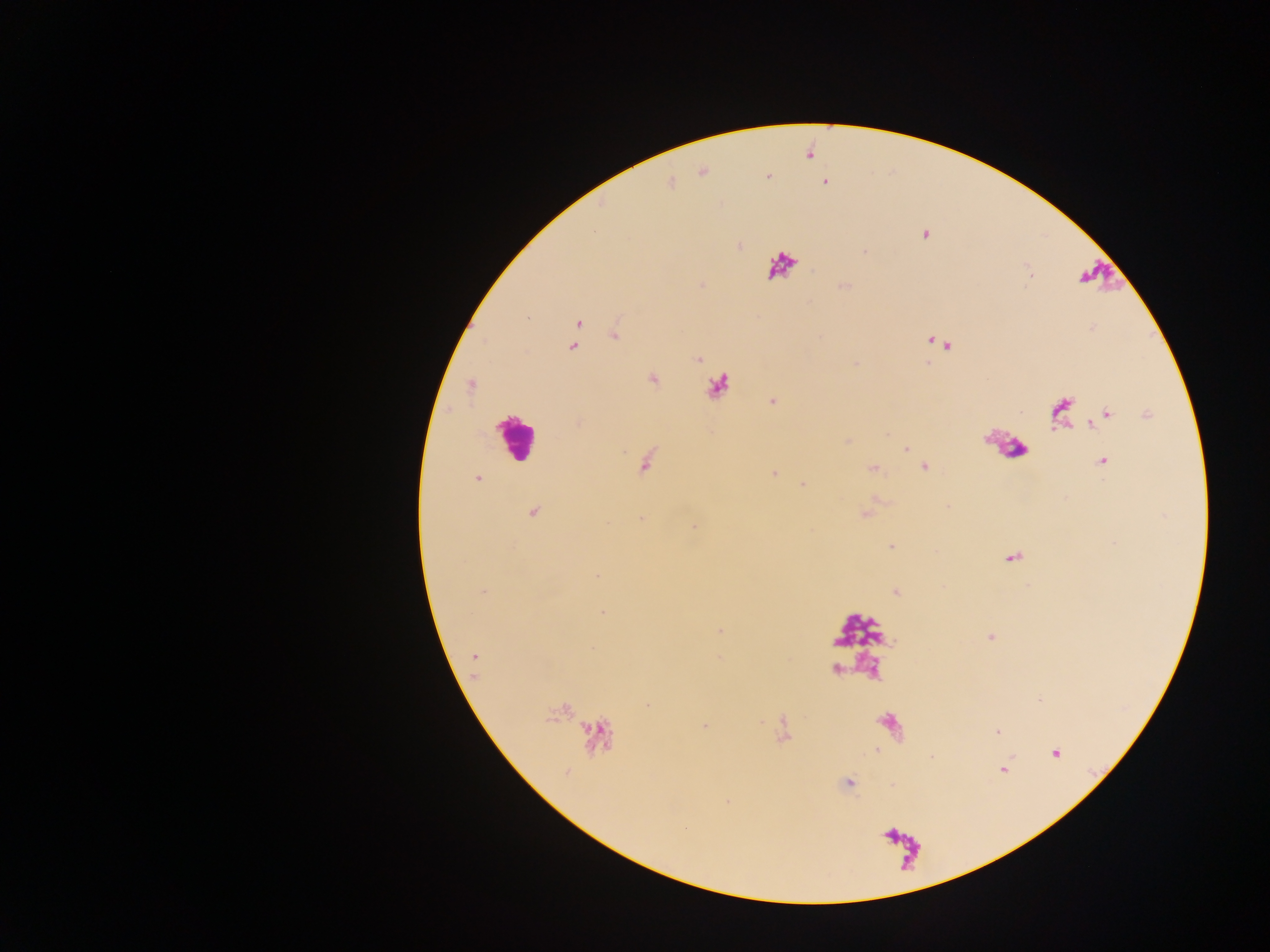
Approximate centers as x y in pixels.
Summary:
  - Leukocyte locations: 516 436
  - Malaria parasite locations: 701 172; 767 176; 824 181; 669 183; 924 234; 740 246; 844 285; 578 322; 615 333; 935 341; 944 344; 572 346; 697 359; 653 378; 471 385; 773 401; 1061 412; 1107 415; 1148 415; 846 440; 906 449; 1102 461; 646 462; 925 466; 872 468; 773 472; 478 478; 803 485; 533 511; 865 513; 641 519; 693 526; 891 546; 1012 558; 597 574; 895 591; 601 612; 719 630; 990 636; 474 656; 647 705; 703 725; 996 732; 1055 753; 931 757; 1003 769; 848 783
  - Image size: 1270×952 pixels
  - Field of view: single
  - Country: Ghana
  - Capture: mobile-phone photograph through a microscope
  - Preparation: thick blood film